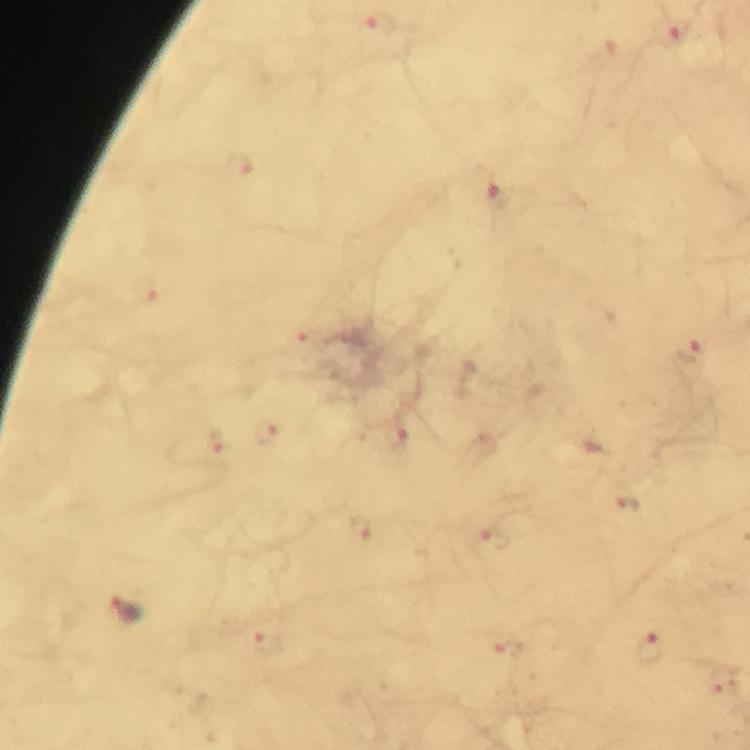 Approximate centers as [x, y] in pixels. Plasmodium parasite locations: [383, 22], [674, 33], [240, 164], [501, 194], [146, 290], [302, 336], [691, 355], [269, 431], [399, 436], [216, 444], [630, 501], [362, 525], [494, 538], [127, 608], [268, 642], [652, 646], [509, 647]. Giemsa stain. Image is 750×750 pixels. Cropped region of a single field of view. Photographed with a smartphone mounted on the microscope. Immersion oil applied. From a diagnostic examination for malaria. Thick blood smear. At 100x magnification.